Locate every blood parasite and identify its species.
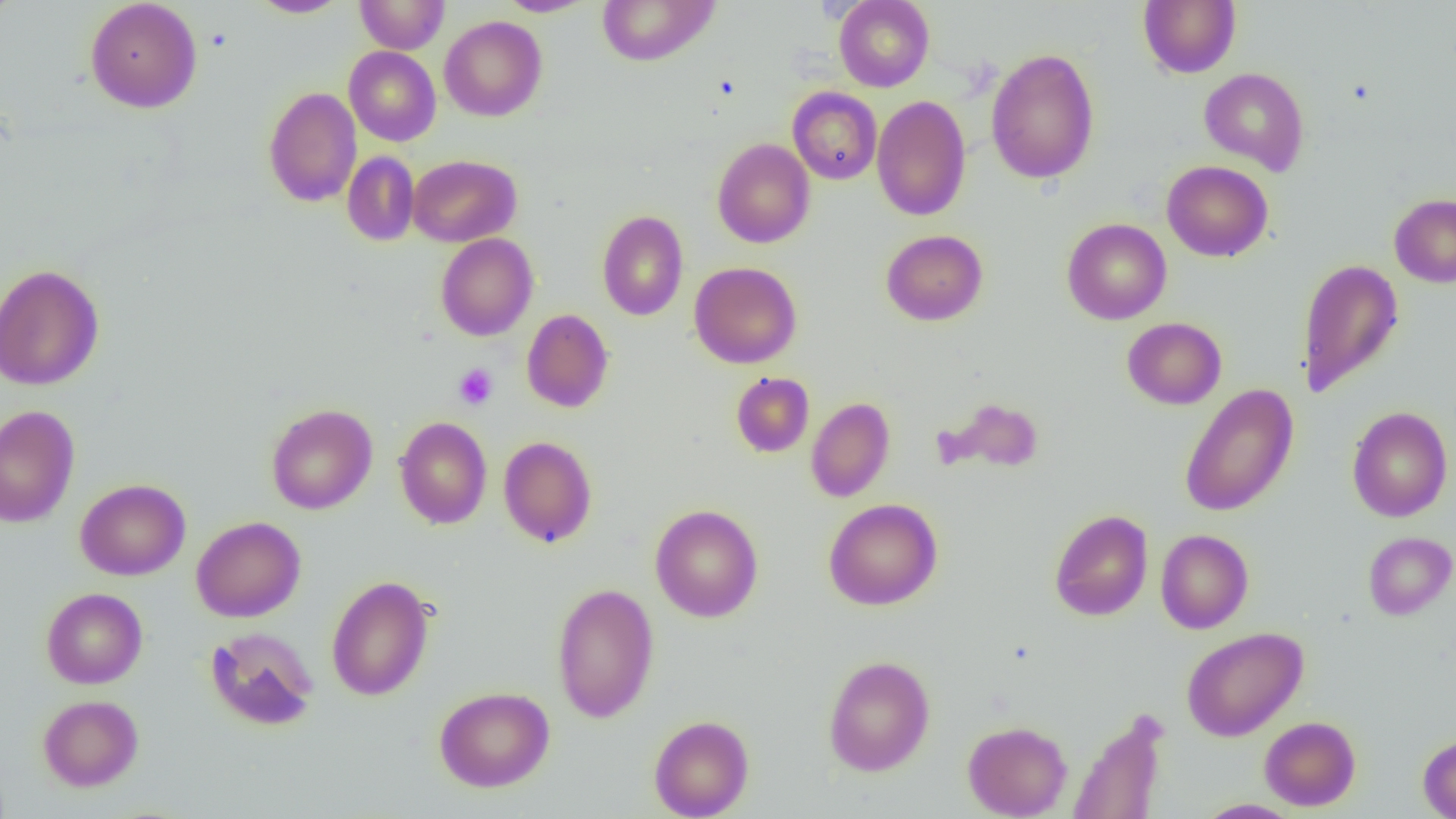
No blood parasites seen.

{
  "slide_level_diagnosis": "no evidence of blood parasites",
  "platelet_locations": "approximate bounding boxes as (x1,y1)-(x2,y2) corner pairs in pixels: (453,364)-(498,410)",
  "field_of_view": "single",
  "uninfected_red_blood_cell_locations": "approximate bounding boxes as (x1,y1)-(x2,y2) corner pairs in pixels: (85,0)-(202,113), (355,0)-(449,54), (495,0)-(597,17), (596,0)-(721,66), (834,0)-(934,91), (1139,0)-(1240,78), (249,1)-(351,18), (439,15)-(547,121), (344,46)-(441,146), (985,48)-(1100,184), (1199,68)-(1309,174), (264,86)-(362,207), (788,87)-(882,185), (871,95)-(971,221), (712,139)-(815,248), (342,151)-(420,246), (408,155)-(521,246), (1162,160)-(1273,262), (1389,193)-(1456,287), (597,210)-(688,320), (1062,218)-(1172,324), (881,230)-(988,325), (436,233)-(538,341), (1298,258)-(1404,398), (689,261)-(801,368), (0,263)-(104,391), (521,308)-(613,413), (1122,317)-(1227,409), (731,372)-(814,457), (1179,383)-(1299,517), (937,396)-(1046,475), (806,397)-(895,502), (266,403)-(377,514), (0,405)-(80,528), (1347,406)-(1453,522), (394,416)-(492,529), (498,436)-(597,547), (75,478)-(190,580), (823,498)-(943,610), (650,504)-(763,622), (1049,509)-(1154,621), (192,516)-(306,622), (1155,529)-(1254,633), (1363,531)-(1456,620), (326,575)-(434,701), (552,582)-(659,723), (42,587)-(147,689), (205,626)-(319,731), (1181,626)-(1307,742), (823,655)-(935,776), (434,686)-(554,792), (38,694)-(143,791), (1069,709)-(1169,819), (649,714)-(754,818), (1259,716)-(1361,811), (963,720)-(1072,818), (1418,734)-(1456,818), (1193,799)-(1302,818)",
  "preparation": "thin blood smear",
  "modality": "light microscopy",
  "image_size": "1456×819 pixels",
  "magnification": "1000x"
}